Outline each uninfected red blood cell.
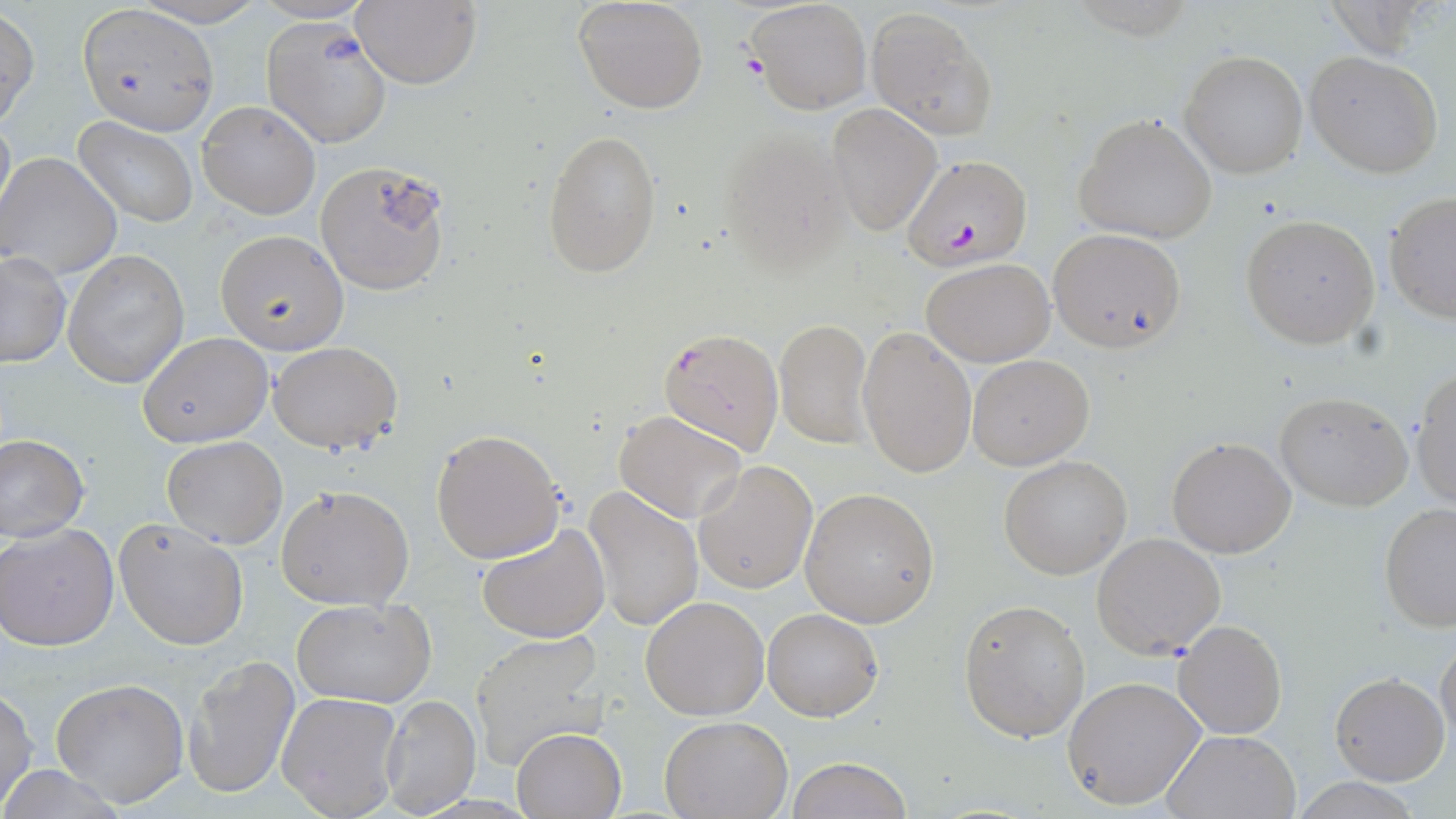

Approximate bounding boxes as (x1,y1)-(x2,y2) corner pairs in pixels.
Uninfected red blood cells: (573,0)-(711,114), (745,0)-(873,115), (350,2)-(482,89), (77,5)-(216,134), (865,6)-(996,137), (0,8)-(39,128), (262,17)-(391,148), (1180,51)-(1308,178), (1304,51)-(1443,178), (197,100)-(320,219), (826,105)-(941,235), (1074,112)-(1220,245), (72,118)-(198,226), (715,125)-(853,276), (542,127)-(662,278), (1,152)-(123,278), (314,159)-(453,296), (1383,193)-(1456,323), (1240,215)-(1381,348), (1047,228)-(1188,353), (215,229)-(347,353), (63,251)-(189,388), (1,253)-(72,368), (922,258)-(1056,367), (775,319)-(873,447), (856,324)-(977,479), (137,331)-(273,448), (267,341)-(403,453), (966,354)-(1094,470), (1409,368)-(1456,511), (1274,389)-(1415,512), (614,411)-(749,525), (430,427)-(566,564), (0,433)-(90,542), (161,436)-(288,549), (1167,437)-(1296,557), (999,455)-(1133,579), (693,461)-(817,594), (276,484)-(416,610), (583,485)-(704,631), (799,488)-(940,627), (1378,501)-(1456,633), (114,516)-(250,650), (476,521)-(610,643), (0,523)-(119,651), (1091,533)-(1227,660), (291,596)-(438,708), (639,596)-(768,720), (958,598)-(1091,743), (762,608)-(884,721), (1173,618)-(1288,738), (469,631)-(610,770), (1436,633)-(1456,749), (186,655)-(301,800), (1330,671)-(1449,786), (1063,676)-(1207,811), (51,677)-(190,809), (1,689)-(39,810), (276,691)-(404,818), (377,692)-(480,818), (659,716)-(791,818), (512,728)-(625,817), (1159,730)-(1302,819), (786,757)-(914,818), (0,764)-(128,818), (1289,778)-(1428,817).

Plasmodium falciparum-infected red blood cell locations: (903,154)-(1032,272), (658,325)-(785,454). Platelet locations: (738,54)-(766,80). Slide-level diagnosis: Plasmodium falciparum. Captured at 1000x magnification. Optical microscopy. One field of a larger specimen. Image is 1456×819 pixels. May-Grünwald-Giemsa-stained preparation. Thin blood smear.